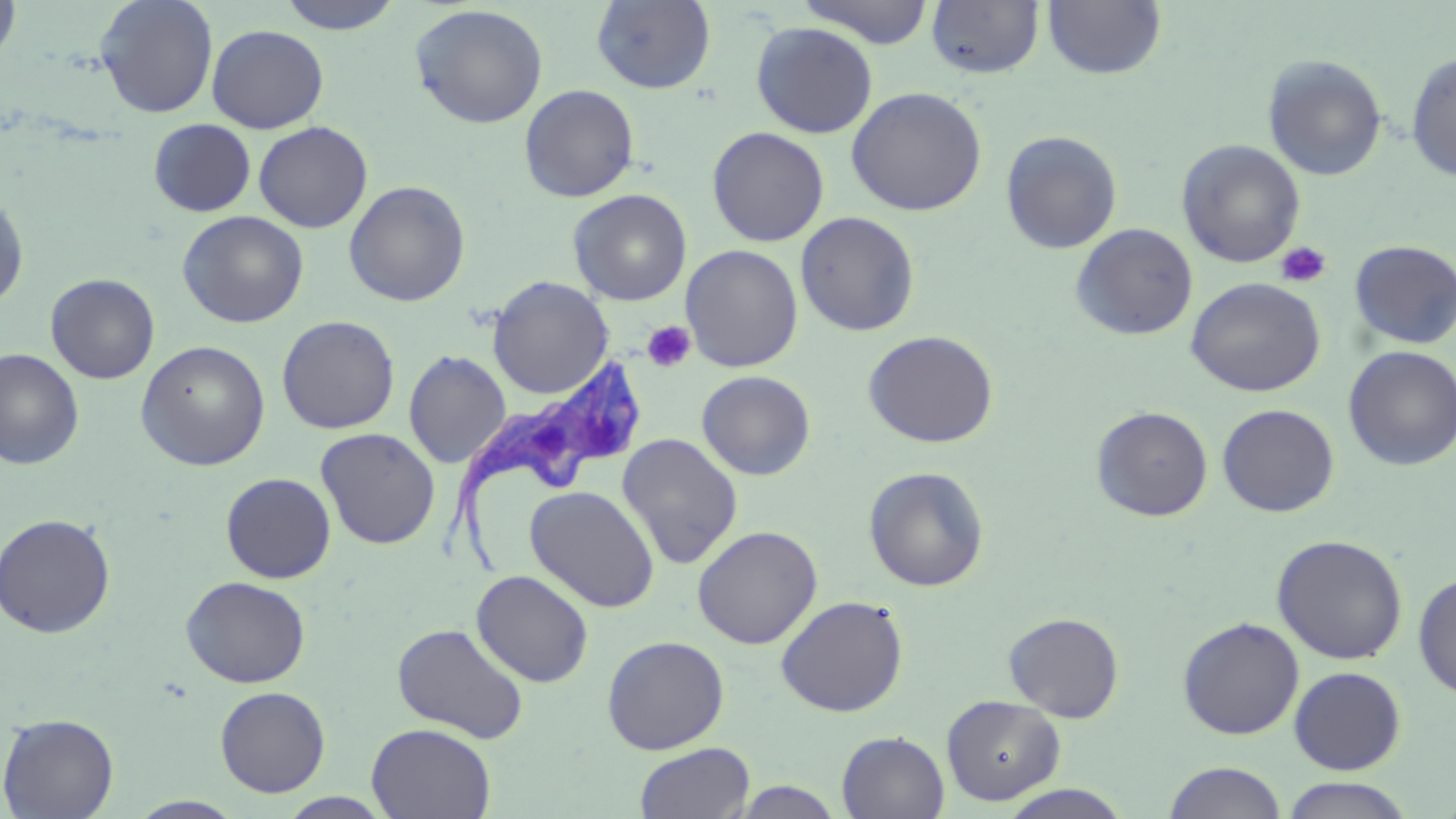
Approximate bounding boxes as (x1,y1)-(x2,y2) corner pairs in pixels. Trypanosoma brucei locations: (434,352)-(639,579). Platelet locations: (1275,241)-(1332,288), (642,320)-(696,373). Uninfected red blood cell locations: (0,0)-(22,72), (94,0)-(219,118), (276,0)-(405,34), (797,0)-(936,48), (1041,0)-(1167,80), (591,1)-(716,93), (925,1)-(1045,79), (409,4)-(548,129), (751,21)-(878,138), (207,24)-(329,133), (1405,50)-(1456,182), (1263,55)-(1387,181), (520,84)-(639,201), (846,86)-(987,216), (148,119)-(256,217), (254,121)-(373,233), (707,126)-(830,246), (1000,130)-(1122,254), (1177,139)-(1306,268), (344,180)-(470,307), (568,189)-(692,305), (0,190)-(29,309), (177,210)-(309,328), (795,211)-(921,336), (1071,223)-(1198,341), (1350,240)-(1456,350), (680,244)-(803,372), (45,273)-(159,384), (488,276)-(614,399), (1185,277)-(1326,397), (276,315)-(400,434), (862,330)-(999,448), (135,340)-(271,471), (1343,345)-(1456,471), (0,349)-(84,470), (403,350)-(511,468), (697,370)-(816,480), (1217,404)-(1339,517), (1091,406)-(1213,521), (315,427)-(441,549), (617,433)-(743,570), (863,466)-(990,592), (221,472)-(336,583), (525,485)-(660,613), (0,513)-(116,639), (692,525)-(823,649), (1271,534)-(1408,665), (472,570)-(594,687), (1413,573)-(1456,701), (181,576)-(311,688), (775,595)-(909,717), (1003,612)-(1125,722), (1176,616)-(1304,739), (392,622)-(529,744), (602,635)-(729,754), (1288,666)-(1407,775), (214,686)-(330,797), (941,694)-(1065,805), (1,713)-(119,818), (366,723)-(496,819), (837,731)-(950,819), (634,742)-(755,819), (1162,761)-(1289,819), (1278,777)-(1417,818), (727,780)-(848,818), (997,784)-(1135,818), (277,793)-(395,818), (128,796)-(247,818). Slide-level diagnosis: Trypanosoma brucei. Captured at 1000x magnification. Optical microscopy. Single field of view. May-Grünwald-Giemsa stain. Thin blood film. Image is 1456×819 pixels.